Identify the blood parasite species.
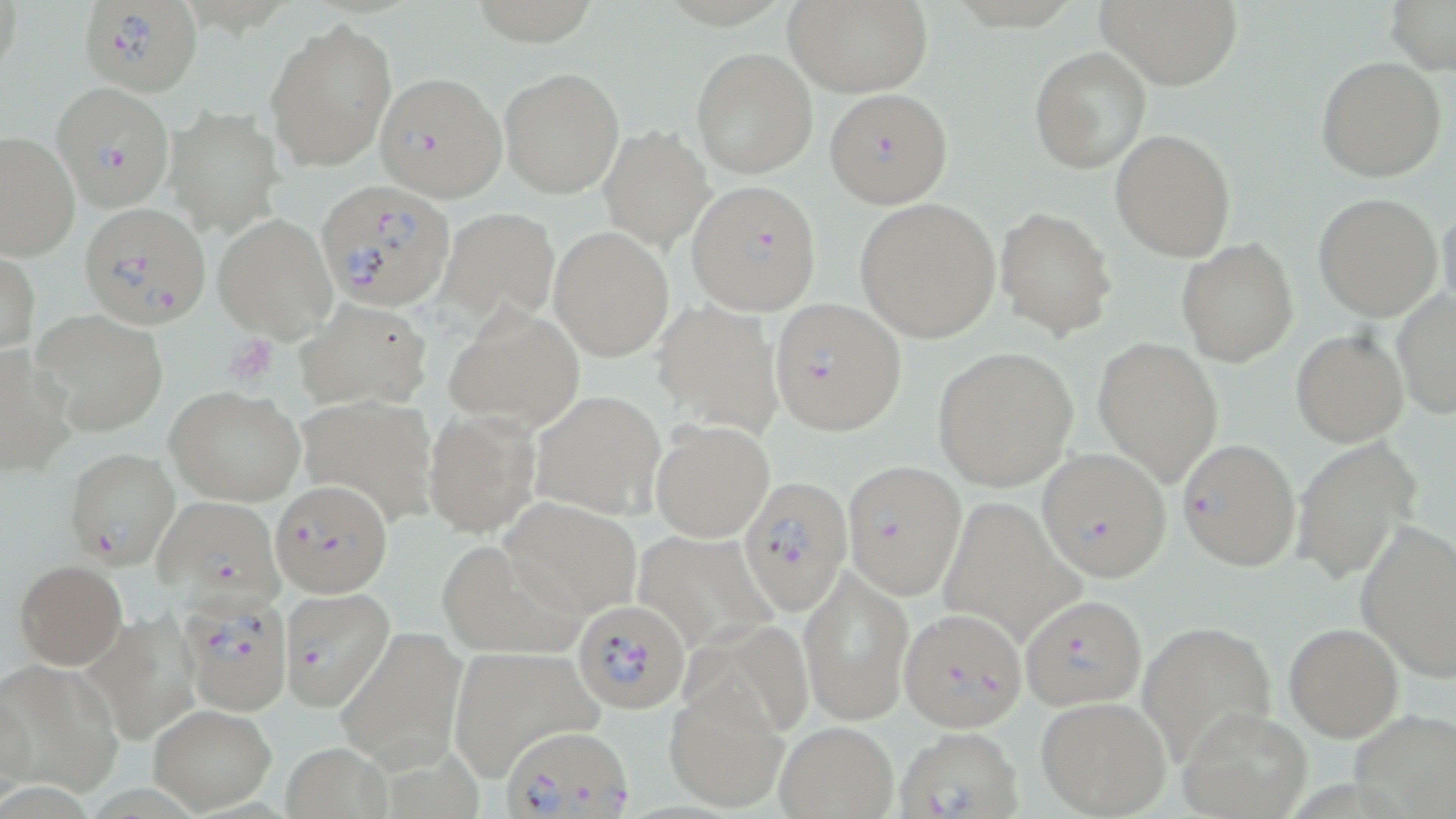

Plasmodium falciparum.

Summary:
  - Coordinate format: approximate bounding boxes as named x1/y1/x2/y2 corners in pixels
  - Platelet locations: (x1=232, y1=342, x2=276, y2=381)
  - Uninfected red blood cell locations: (x1=785, y1=0, x2=933, y2=97), (x1=1093, y1=0, x2=1245, y2=91), (x1=1385, y1=0, x2=1456, y2=75), (x1=267, y1=15, x2=398, y2=173), (x1=691, y1=46, x2=818, y2=180), (x1=1029, y1=46, x2=1151, y2=175), (x1=1315, y1=57, x2=1447, y2=182), (x1=498, y1=65, x2=624, y2=197), (x1=167, y1=104, x2=285, y2=235), (x1=598, y1=124, x2=717, y2=254), (x1=1110, y1=129, x2=1236, y2=262), (x1=0, y1=130, x2=79, y2=262), (x1=1313, y1=192, x2=1444, y2=322), (x1=854, y1=198, x2=1001, y2=344), (x1=1436, y1=201, x2=1456, y2=323), (x1=995, y1=206, x2=1116, y2=341), (x1=437, y1=207, x2=561, y2=327), (x1=212, y1=211, x2=339, y2=343), (x1=549, y1=225, x2=675, y2=362), (x1=1176, y1=239, x2=1301, y2=365), (x1=1, y1=249, x2=40, y2=355), (x1=1392, y1=290, x2=1455, y2=419), (x1=294, y1=297, x2=433, y2=411), (x1=652, y1=301, x2=782, y2=436), (x1=445, y1=307, x2=584, y2=432), (x1=31, y1=308, x2=170, y2=437), (x1=1290, y1=329, x2=1408, y2=446), (x1=1090, y1=335, x2=1224, y2=486), (x1=932, y1=347, x2=1078, y2=492), (x1=0, y1=350, x2=75, y2=479), (x1=164, y1=385, x2=306, y2=506), (x1=531, y1=388, x2=668, y2=521), (x1=424, y1=408, x2=541, y2=539), (x1=650, y1=420, x2=776, y2=542), (x1=1293, y1=437, x2=1421, y2=586), (x1=500, y1=497, x2=643, y2=618), (x1=1354, y1=520, x2=1456, y2=684), (x1=434, y1=535, x2=590, y2=662), (x1=12, y1=559, x2=128, y2=670), (x1=798, y1=567, x2=909, y2=724), (x1=82, y1=612, x2=208, y2=747), (x1=1139, y1=620, x2=1278, y2=764), (x1=1281, y1=621, x2=1404, y2=742), (x1=337, y1=629, x2=468, y2=772), (x1=445, y1=649, x2=601, y2=777), (x1=0, y1=658, x2=123, y2=796), (x1=663, y1=683, x2=786, y2=813), (x1=1035, y1=695, x2=1171, y2=818), (x1=148, y1=702, x2=277, y2=812), (x1=1180, y1=707, x2=1312, y2=819), (x1=1351, y1=707, x2=1454, y2=817), (x1=774, y1=720, x2=898, y2=817), (x1=282, y1=740, x2=393, y2=818)
  - Plasmodium falciparum-infected red blood cell locations: (x1=78, y1=0, x2=203, y2=97), (x1=376, y1=71, x2=508, y2=202), (x1=51, y1=82, x2=176, y2=212), (x1=824, y1=89, x2=953, y2=209), (x1=688, y1=181, x2=822, y2=316), (x1=316, y1=183, x2=454, y2=314), (x1=79, y1=202, x2=212, y2=331), (x1=768, y1=298, x2=907, y2=435), (x1=1176, y1=437, x2=1301, y2=573), (x1=63, y1=447, x2=180, y2=570), (x1=1037, y1=448, x2=1171, y2=582), (x1=841, y1=459, x2=967, y2=600), (x1=737, y1=476, x2=850, y2=613), (x1=272, y1=481, x2=391, y2=598), (x1=151, y1=495, x2=283, y2=605), (x1=282, y1=585, x2=397, y2=714), (x1=179, y1=592, x2=293, y2=713), (x1=1020, y1=592, x2=1148, y2=711), (x1=572, y1=599, x2=689, y2=712), (x1=900, y1=608, x2=1027, y2=732), (x1=505, y1=725, x2=632, y2=819), (x1=892, y1=725, x2=1025, y2=819)
  - Image size: 1456×819 pixels
  - Magnification: 1000x
  - Field of view: single
  - Preparation: thin blood film
  - Modality: optical microscopy
  - Stain: May-Grünwald-Giemsa